Classify this cell by malaria status.
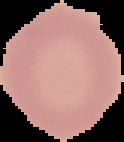
Uninfected.

image size = 124×142 pixels
image type = cell region segmented out of the field of view; surrounding area masked to black
preparation = thin blood film